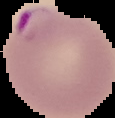

Cell region segmented out of the field of view; the surrounding area is masked to black. Result: Plasmodium parasites detected. From a thin blood film. Image is 115×118 pixels.